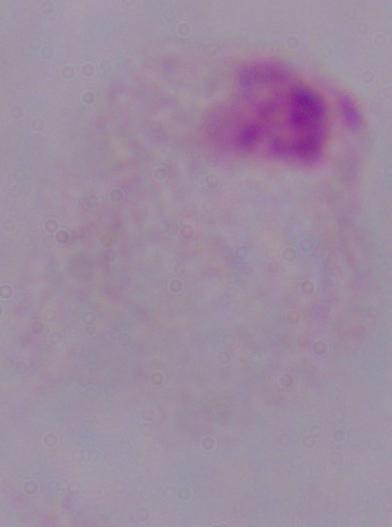

modality = photomicrograph
magnification = 1000x
identification = trichomonad